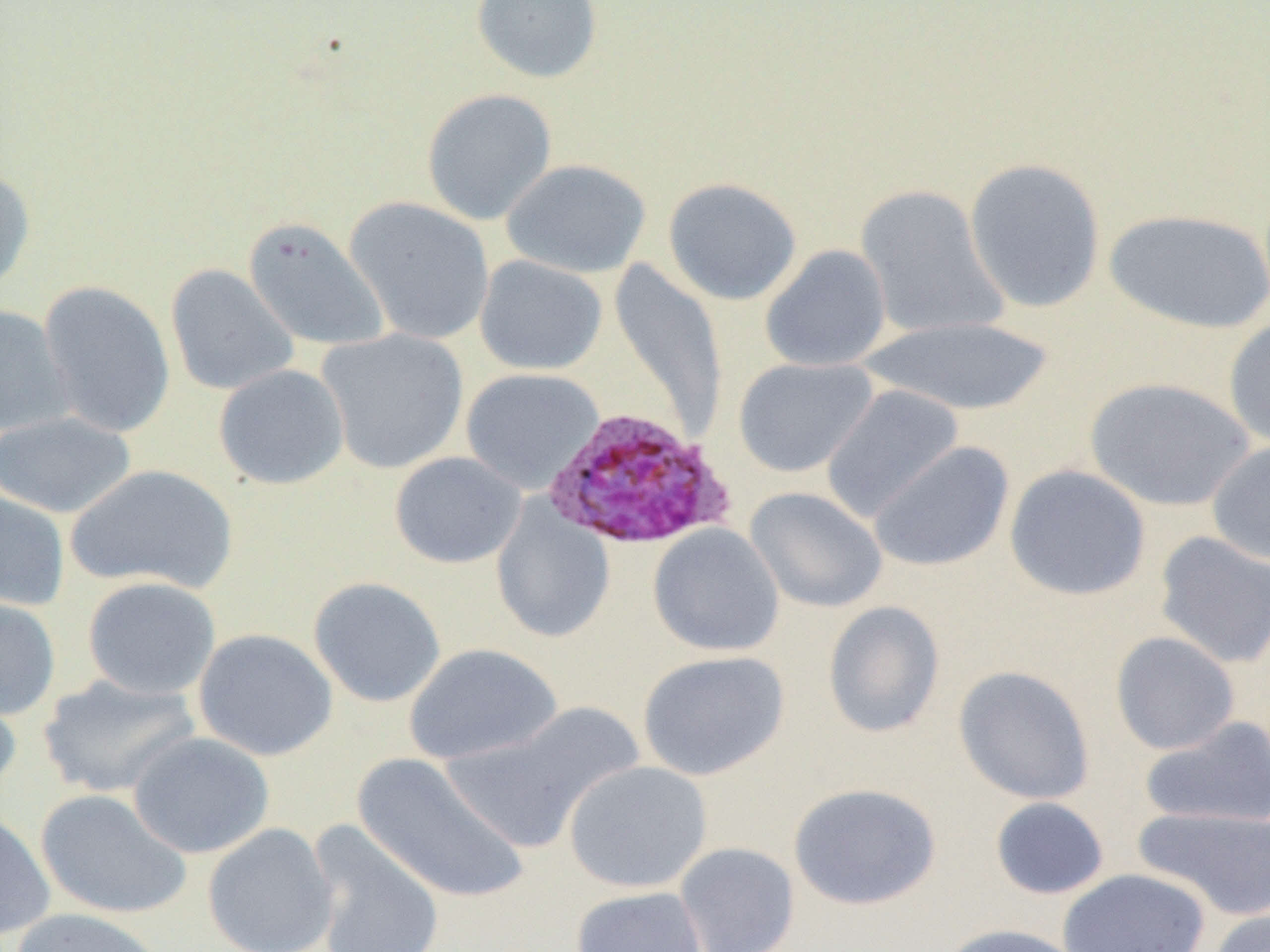
Summary:
  - Coordinate format: approximate bounding boxes as (x1,y1)-(x2,y2) corner pairs in pixels
  - Uninfected red blood cell locations: (470,0)-(603,84), (421,88)-(557,225), (501,158)-(651,278), (964,158)-(1107,313), (0,164)-(35,297), (663,177)-(802,305), (854,184)-(1009,340), (345,196)-(495,345), (1104,207)-(1270,334), (243,217)-(389,351), (760,244)-(891,372), (474,255)-(608,376), (609,260)-(727,438), (165,263)-(299,396), (37,280)-(175,438), (0,303)-(74,437), (1223,316)-(1270,449), (861,317)-(1055,416), (317,328)-(469,474), (733,357)-(878,477), (213,364)-(349,490), (460,367)-(604,494), (1083,376)-(1255,512), (820,383)-(964,522), (0,410)-(136,519), (867,440)-(1015,573), (1206,440)-(1270,566), (389,451)-(526,569), (67,463)-(238,594), (1004,464)-(1151,601), (745,486)-(888,613), (0,489)-(70,612), (490,498)-(616,644), (648,523)-(784,657), (1153,531)-(1270,669), (81,576)-(221,699), (308,576)-(446,707), (0,595)-(61,722), (822,600)-(945,739), (193,628)-(338,761), (1110,631)-(1240,756), (402,643)-(562,765), (636,650)-(790,781), (953,665)-(1095,805), (36,673)-(201,799), (0,678)-(23,804), (438,703)-(645,854), (1139,715)-(1270,830), (127,731)-(275,859), (351,752)-(530,905), (563,760)-(713,893), (787,782)-(941,910), (35,788)-(192,920), (990,796)-(1109,900), (1133,805)-(1270,920), (0,806)-(56,943), (306,819)-(445,952), (202,823)-(339,952), (674,842)-(800,952), (1057,868)-(1210,952), (570,886)-(709,952), (10,907)-(169,952), (1206,909)-(1270,952), (938,922)-(1086,952)
  - Plasmodium ovale-infected red blood cell locations: (543,407)-(735,551)
  - Slide-level diagnosis: Plasmodium ovale
  - Preparation: thin blood film
  - Field of view: one of a larger specimen
  - Modality: optical microscopy
  - Image size: 1270×952 pixels
  - Magnification: 1000x